Give the position of every Plasmodium parasite visible.
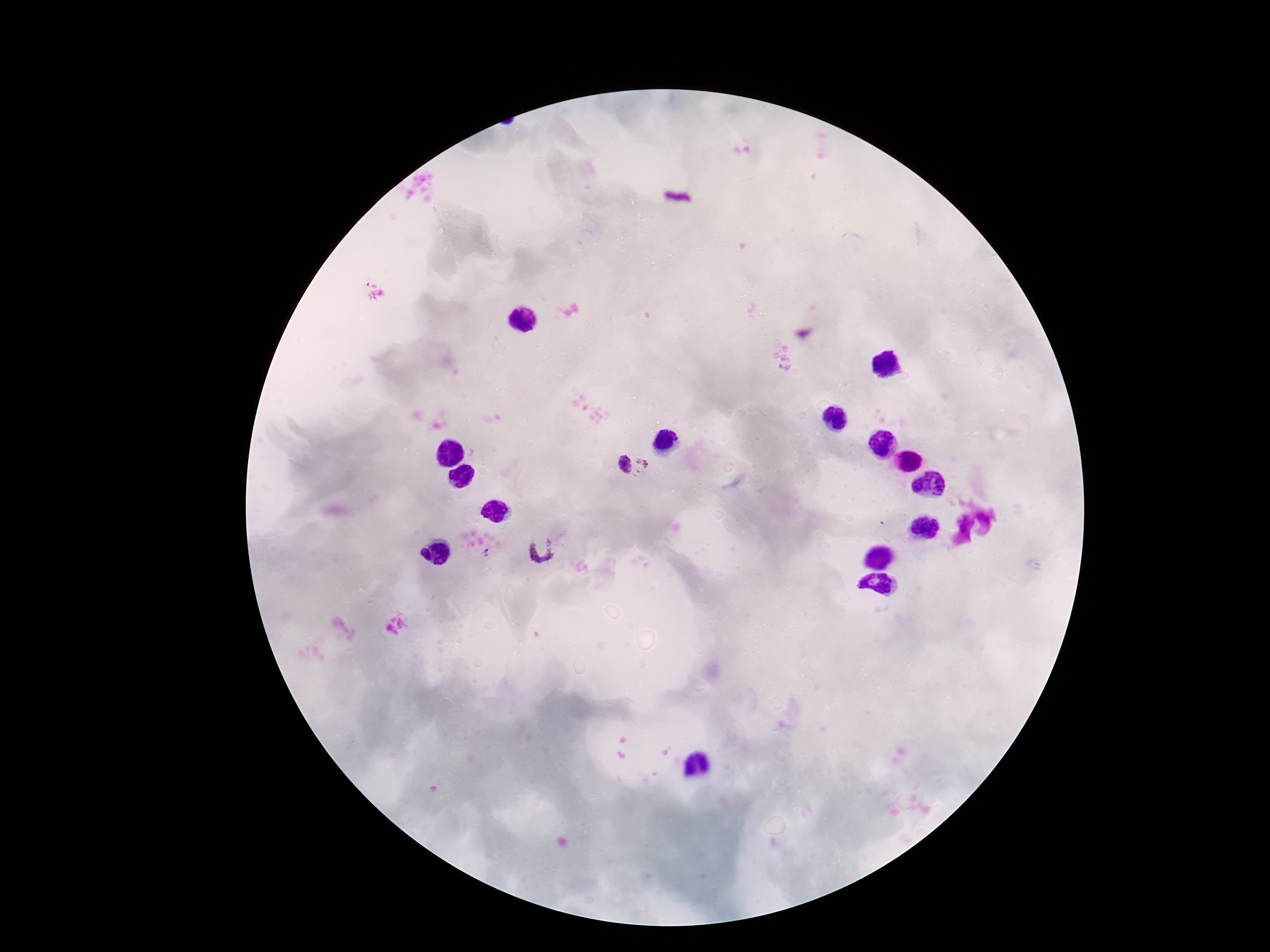
Approximate centers as (x, y) in pixels.
Plasmodium parasites: (623, 463), (645, 466), (543, 548), (487, 552).

image size = 1270×952 pixels
stain = Giemsa
capture = smartphone camera through the microscope eyepiece
magnification = 100x
field of view = one from this slide
patient malaria status = positive
preparation = thick blood film